Classify this cell by malaria status.
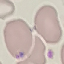

It is parasitized.

Thin blood film. Acquired by smartphone through the microscope eyepiece. Automatically extracted cell patch, resized to 64 × 64 pixels. Giemsa-stained preparation.